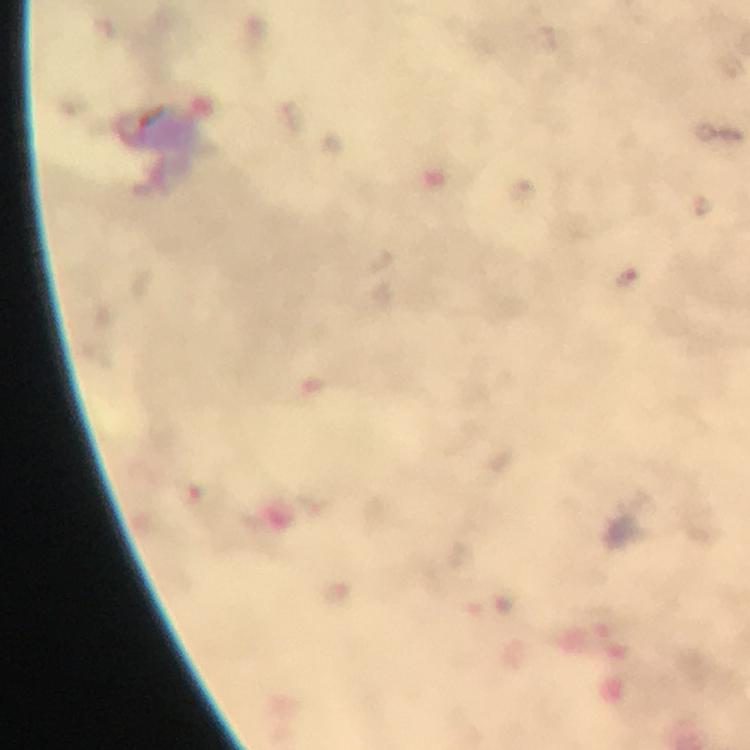
Approximate centers as (x, y) in pixels.
Summary:
  - Malaria parasite locations: (628, 278)
  - Cropped from: a single field of view
  - Context: from a malaria diagnostic workup
  - Stain: Giemsa
  - Immersion oil: applied
  - Capture: smartphone camera through the microscope
  - Image size: 750×750 pixels
  - Magnification: 100x
  - Preparation: thick blood film